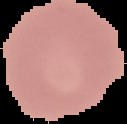

result = no malaria parasites detected
image size = 127×124 pixels
preparation = thin blood film
image type = segmented cell region on a black background